Outline each Plasmodium vivax-infected red blood cell.
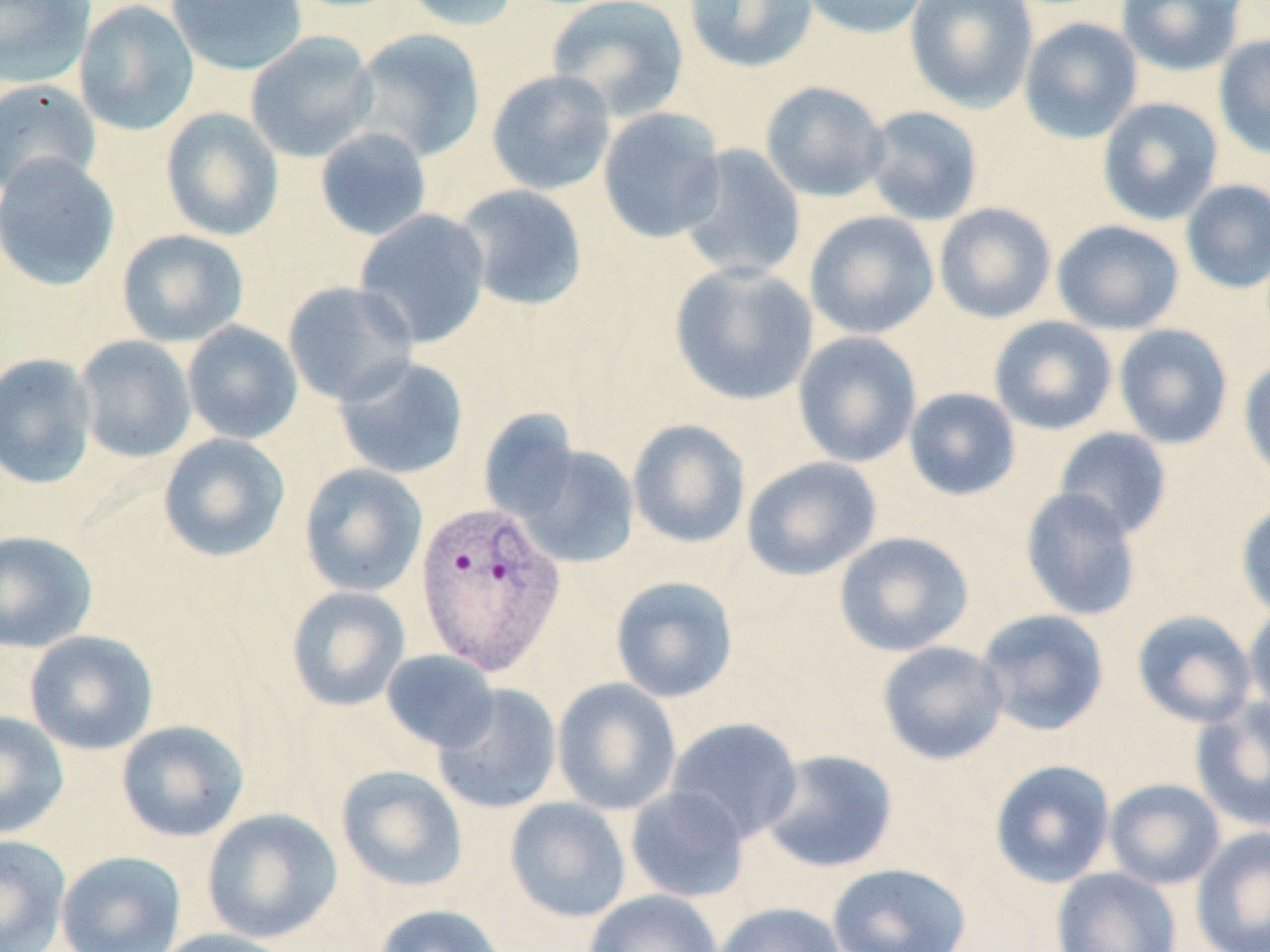

Approximate bounding boxes as [x1, y1, x2, y2] in pixels.
Plasmodium vivax-infected red blood cells: [413, 499, 567, 676].

Summary:
  - Uninfected red blood cell locations: [0, 0, 96, 89], [74, 0, 200, 136], [166, 0, 308, 76], [400, 0, 523, 32], [545, 0, 690, 122], [683, 0, 819, 74], [796, 0, 932, 39], [904, 0, 1039, 113], [1116, 0, 1246, 76], [1018, 17, 1143, 143], [351, 28, 486, 161], [244, 31, 378, 163], [1213, 34, 1270, 160], [486, 69, 617, 196], [0, 79, 100, 197], [760, 80, 890, 203], [1097, 97, 1223, 226], [861, 105, 983, 226], [160, 107, 284, 241], [597, 107, 726, 244], [314, 127, 432, 241], [677, 144, 806, 281], [0, 153, 121, 291], [1180, 179, 1270, 294], [454, 184, 588, 312], [933, 203, 1056, 324], [353, 209, 492, 348], [804, 210, 939, 340], [1051, 220, 1185, 335], [116, 229, 250, 348], [668, 262, 818, 406], [282, 281, 419, 407], [988, 316, 1118, 435], [181, 320, 303, 445], [1113, 323, 1233, 450], [793, 331, 922, 468], [74, 335, 197, 463], [0, 352, 98, 490], [333, 355, 470, 480], [1238, 358, 1270, 487], [903, 387, 1021, 501], [627, 419, 751, 549], [1053, 426, 1173, 540], [157, 433, 290, 562], [500, 437, 641, 570], [741, 456, 882, 581], [299, 463, 428, 597], [1019, 487, 1142, 621], [1236, 501, 1270, 621], [0, 529, 98, 653], [833, 531, 974, 657], [609, 575, 738, 703], [285, 586, 411, 712], [1243, 604, 1270, 721], [975, 608, 1110, 736], [1132, 610, 1257, 729], [24, 630, 159, 755], [876, 640, 1009, 765], [380, 650, 501, 753], [552, 678, 682, 815], [433, 683, 562, 814], [1191, 696, 1270, 833], [0, 711, 69, 839], [666, 717, 803, 844], [115, 720, 249, 842], [760, 748, 898, 874], [989, 759, 1116, 888], [335, 765, 468, 892], [1104, 778, 1226, 890], [625, 786, 749, 903], [504, 796, 631, 923], [201, 807, 343, 944], [1190, 826, 1270, 952], [0, 834, 71, 952], [56, 850, 186, 952], [827, 862, 971, 952], [1051, 867, 1182, 952], [583, 889, 723, 952], [715, 901, 846, 952], [374, 903, 509, 952], [152, 928, 291, 952]
  - Slide-level diagnosis: Plasmodium vivax
  - Magnification: 1000x
  - Stain: May-Grünwald-Giemsa
  - Field of view: single
  - Modality: light microscopy
  - Preparation: thin blood smear
  - Image size: 1270×952 pixels